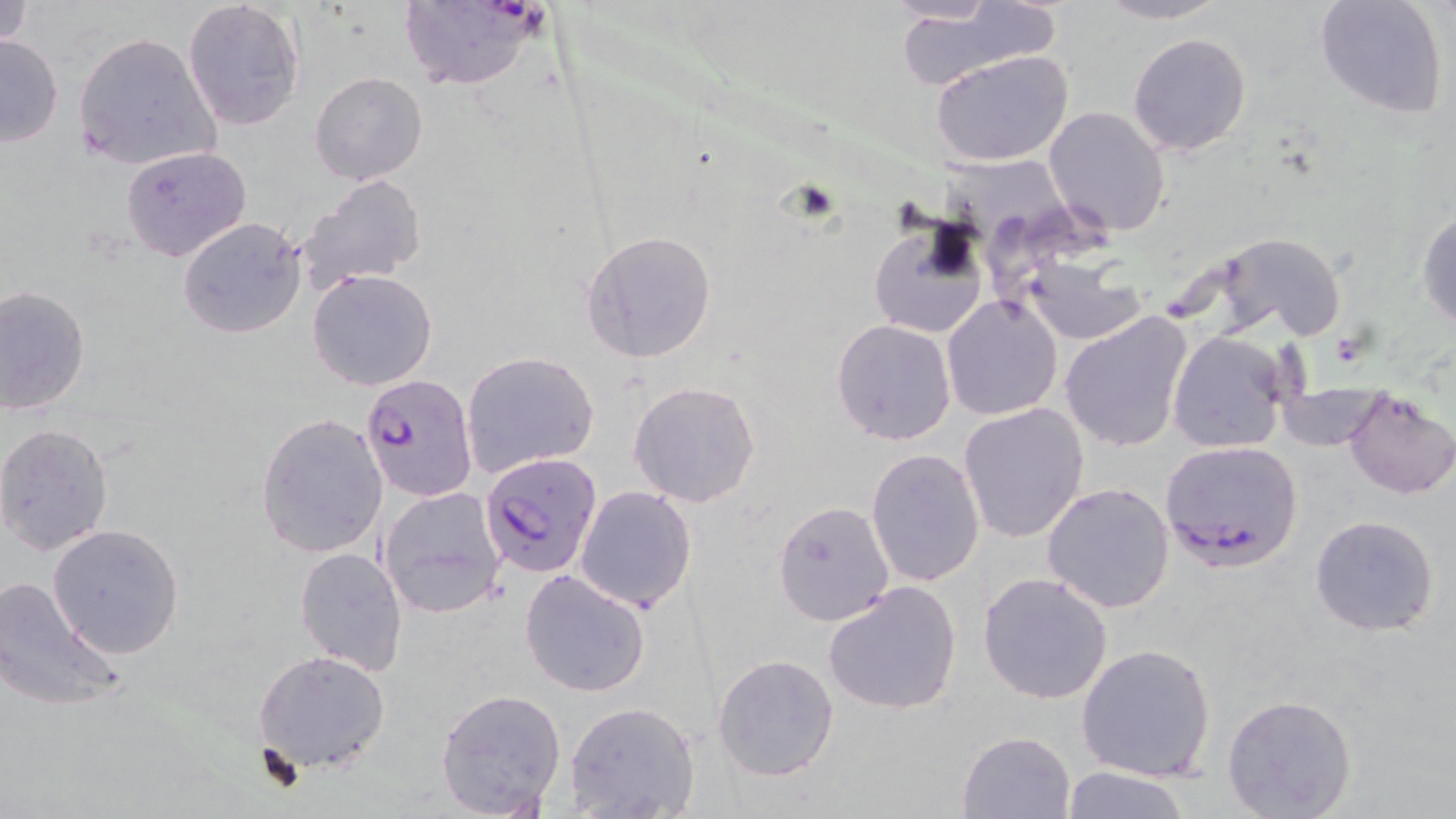
Approximate bounding boxes as named x1/y1/x2/y2 corners in pixels. Uninfected red blood cell locations: (x1=1, y1=0, x2=34, y2=48), (x1=1090, y1=0, x2=1230, y2=24), (x1=1313, y1=0, x2=1449, y2=120), (x1=182, y1=1, x2=308, y2=132), (x1=894, y1=4, x2=1059, y2=87), (x1=73, y1=32, x2=218, y2=169), (x1=1127, y1=32, x2=1252, y2=156), (x1=0, y1=34, x2=64, y2=147), (x1=932, y1=50, x2=1073, y2=166), (x1=310, y1=72, x2=428, y2=186), (x1=1044, y1=106, x2=1171, y2=236), (x1=121, y1=146, x2=251, y2=263), (x1=941, y1=153, x2=1077, y2=272), (x1=298, y1=174, x2=427, y2=290), (x1=1416, y1=204, x2=1456, y2=333), (x1=866, y1=211, x2=988, y2=344), (x1=178, y1=216, x2=306, y2=339), (x1=580, y1=229, x2=718, y2=364), (x1=1199, y1=231, x2=1351, y2=342), (x1=1021, y1=257, x2=1145, y2=345), (x1=307, y1=269, x2=439, y2=390), (x1=0, y1=286, x2=90, y2=414), (x1=941, y1=295, x2=1064, y2=422), (x1=1059, y1=311, x2=1192, y2=452), (x1=831, y1=318, x2=957, y2=445), (x1=1168, y1=330, x2=1291, y2=456), (x1=462, y1=350, x2=599, y2=477), (x1=627, y1=379, x2=762, y2=507), (x1=1340, y1=388, x2=1456, y2=499), (x1=959, y1=404, x2=1090, y2=543), (x1=255, y1=413, x2=387, y2=560), (x1=1, y1=423, x2=117, y2=558), (x1=866, y1=449, x2=984, y2=587), (x1=1042, y1=482, x2=1175, y2=613), (x1=574, y1=485, x2=697, y2=612), (x1=377, y1=486, x2=508, y2=618), (x1=772, y1=500, x2=894, y2=625), (x1=1310, y1=514, x2=1440, y2=636), (x1=46, y1=524, x2=186, y2=659), (x1=295, y1=547, x2=409, y2=675), (x1=519, y1=568, x2=652, y2=698), (x1=977, y1=573, x2=1113, y2=705), (x1=0, y1=574, x2=127, y2=712), (x1=823, y1=581, x2=962, y2=716), (x1=1076, y1=643, x2=1217, y2=782), (x1=253, y1=649, x2=390, y2=776), (x1=712, y1=652, x2=840, y2=781), (x1=435, y1=687, x2=567, y2=816), (x1=1223, y1=694, x2=1356, y2=818), (x1=563, y1=701, x2=699, y2=819), (x1=956, y1=731, x2=1076, y2=818), (x1=1061, y1=765, x2=1193, y2=819). Plasmodium falciparum-infected red blood cell locations: (x1=398, y1=3, x2=545, y2=92), (x1=359, y1=375, x2=477, y2=501), (x1=1159, y1=440, x2=1304, y2=572), (x1=480, y1=450, x2=603, y2=580). Slide-level diagnosis: Plasmodium falciparum. 1000x magnification. One field of a larger specimen. May-Grünwald-Giemsa-stained preparation. Image is 1456×819 pixels. Thin blood film. Light microscopy.